Describe the morphology of the erythrocytes.
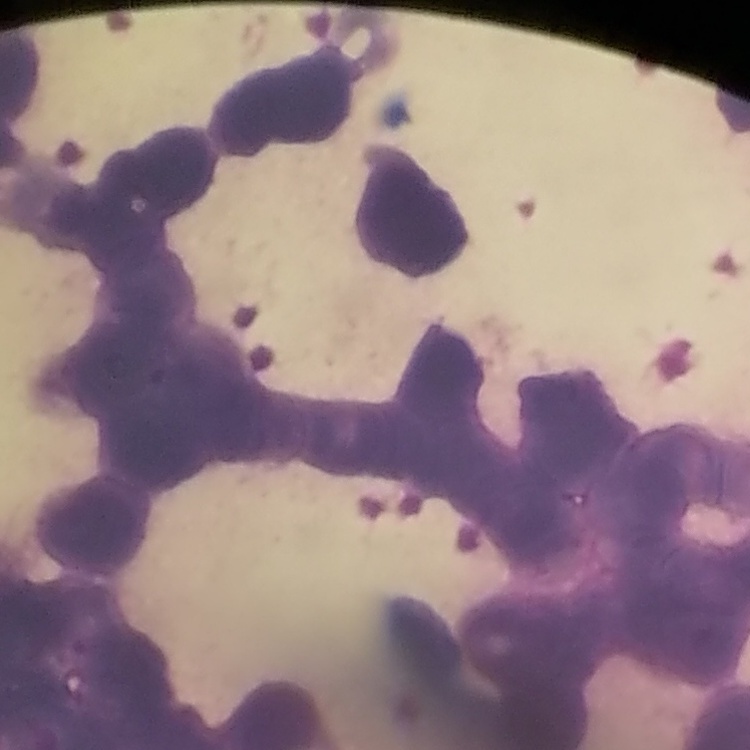

They show rouleaux formation.

preparation = thin peripheral smear
image type = square crop of a larger photomicrograph
stain = Field's or Giemsa